State which parasite is depicted.
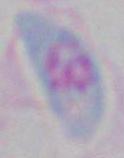

Toxoplasma gondii.

Summary:
  - Magnification: 1000x
  - Modality: photomicrograph